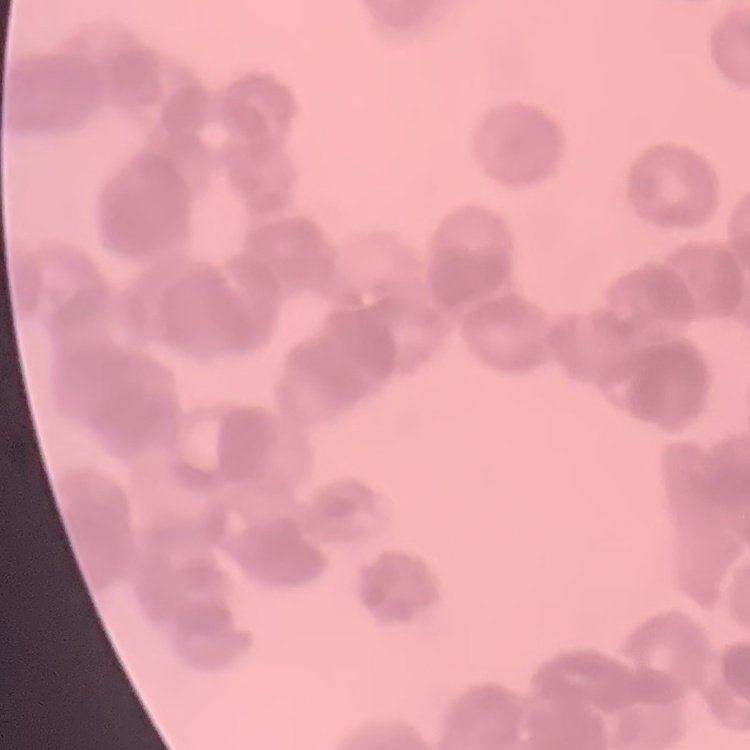
The erythrocytes show rouleaux formation. Field's or Giemsa stain. One tile cut from a larger photomicrograph. Thin blood smear.